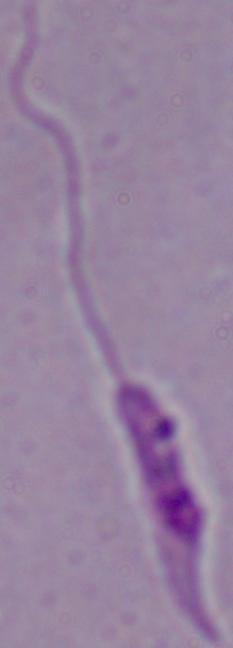

magnification = 1000x
modality = photomicrograph
identification = Leishmania